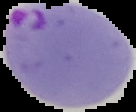

Malaria status: parasitized. Image is 136×112 pixels. Segmented cell region on a black background. From a thin blood film.